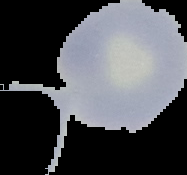 Cell region segmented out of the field of view; the surrounding area is masked to black. Image is 187×175 pixels. Malaria status: uninfected. From a thin blood smear.